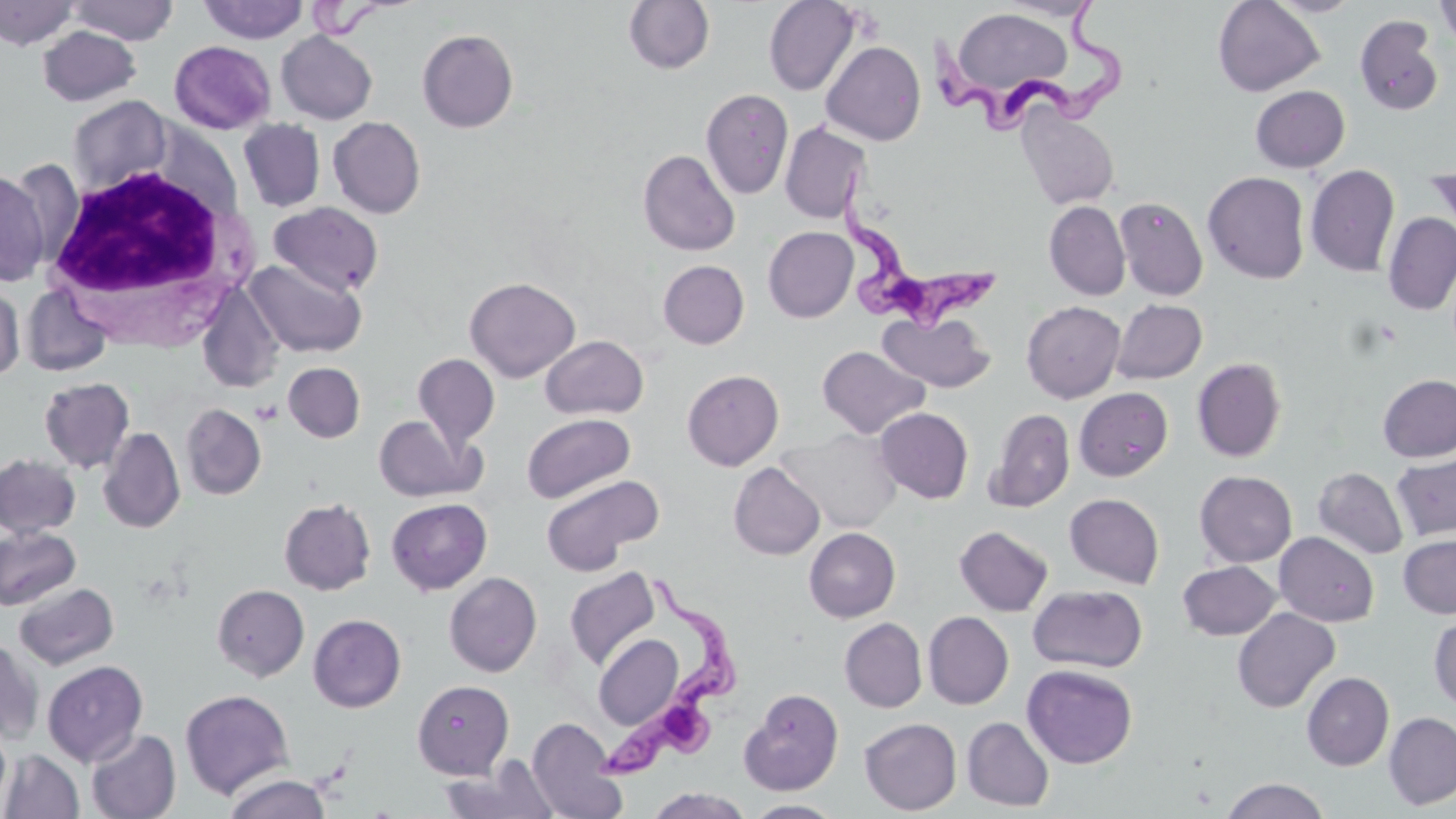
slide-level diagnosis = Trypanosoma brucei
field of view = single
uninfected red blood cell locations = approximate bounding boxes as [x1, y1, x2, y2] in pixels: [67, 0, 179, 44], [623, 0, 714, 74], [763, 0, 860, 96], [996, 0, 1101, 21], [1264, 0, 1364, 17], [1434, 0, 1456, 49], [0, 1, 79, 50], [199, 1, 308, 44], [1213, 1, 1324, 96], [949, 7, 1072, 100], [1354, 15, 1443, 116], [37, 25, 141, 106], [417, 29, 518, 132], [276, 31, 377, 124], [169, 40, 275, 134], [821, 41, 926, 145], [1250, 85, 1350, 173], [701, 89, 794, 200], [67, 95, 174, 195], [1016, 106, 1119, 209], [328, 116, 426, 218], [238, 119, 325, 212], [780, 122, 871, 224], [638, 149, 740, 256], [1306, 164, 1400, 277], [1425, 164, 1456, 242], [0, 169, 49, 286], [1203, 171, 1310, 284], [1114, 196, 1208, 301], [269, 201, 384, 297], [1044, 201, 1131, 300], [1383, 213, 1456, 316], [763, 227, 858, 322], [245, 259, 366, 358], [658, 260, 749, 349], [465, 276, 580, 382], [0, 283, 25, 380], [22, 284, 113, 377], [197, 284, 284, 393], [1110, 299, 1206, 384], [1022, 301, 1126, 402], [878, 311, 996, 392], [540, 335, 649, 419], [817, 344, 930, 439], [413, 353, 500, 450], [1192, 358, 1287, 462], [283, 362, 365, 443], [682, 369, 784, 471], [1378, 374, 1456, 462], [39, 377, 134, 473], [1074, 388, 1172, 481], [181, 404, 266, 500], [875, 407, 973, 503], [987, 408, 1075, 512], [522, 412, 635, 503], [373, 414, 481, 503], [98, 427, 185, 533], [778, 428, 901, 532], [1392, 451, 1456, 542], [0, 454, 80, 538], [729, 462, 825, 560], [1313, 467, 1409, 560], [1194, 470, 1297, 567], [541, 474, 663, 575], [1064, 493, 1164, 588], [279, 498, 376, 595], [386, 498, 492, 595], [954, 525, 1054, 615], [0, 526, 80, 610], [804, 527, 900, 622], [1274, 532, 1379, 626], [1398, 534, 1456, 618], [1178, 560, 1281, 640], [564, 567, 661, 671], [444, 572, 542, 677], [14, 582, 119, 670], [212, 584, 309, 681], [1028, 584, 1148, 673], [1232, 607, 1340, 713], [923, 611, 1013, 709], [308, 614, 406, 712], [1429, 616, 1456, 711], [840, 618, 927, 712], [593, 634, 685, 730], [0, 638, 43, 744], [42, 660, 148, 766], [1022, 664, 1138, 768], [1302, 672, 1394, 770], [412, 680, 513, 779], [739, 688, 843, 796], [179, 689, 295, 800], [1384, 712, 1456, 810], [526, 716, 628, 818], [962, 716, 1054, 812], [859, 717, 962, 815], [0, 722, 11, 810], [85, 728, 181, 818], [1, 749, 84, 818], [441, 758, 561, 819], [222, 773, 332, 818], [1221, 777, 1329, 819], [647, 787, 753, 818], [744, 799, 846, 817]
preparation = thin blood film
white blood cell locations = approximate bounding boxes as [x1, y1, x2, y2] in pixels: [40, 163, 251, 334]
magnification = 1000x
stain = May-Grünwald-Giemsa
Trypanosoma brucei locations = approximate bounding boxes as [x1, y1, x2, y2] in pixels: [922, 0, 1131, 136], [835, 168, 1003, 336], [602, 573, 740, 782]
modality = optical microscopy
platelet locations = approximate bounding boxes as [x1, y1, x2, y2] in pixels: [251, 399, 282, 425]
image size = 1456×819 pixels